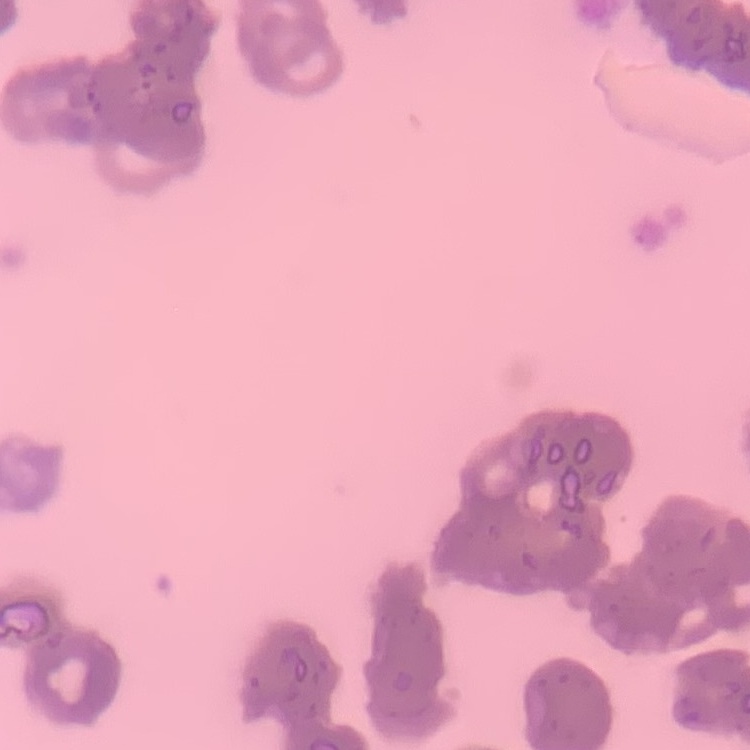
The red blood cells show rouleaux formation. Square crop of a larger photomicrograph. Thin blood film. Field's or Giemsa stain.